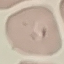

Malaria status: uninfected. Giemsa-stained preparation. Thin blood smear. Acquired by smartphone through the microscope eyepiece. Automatically extracted cell patch, resized to 64 × 64 pixels.